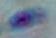
modality: photomicrograph
identification: Toxoplasma gondii
magnification: 1000x